Assess this cell for malaria.
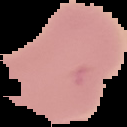

Parasitized.

Summary:
  - Preparation: thin blood film
  - Image type: cell region segmented out of the field of view; surrounding area masked to black
  - Image size: 127×127 pixels